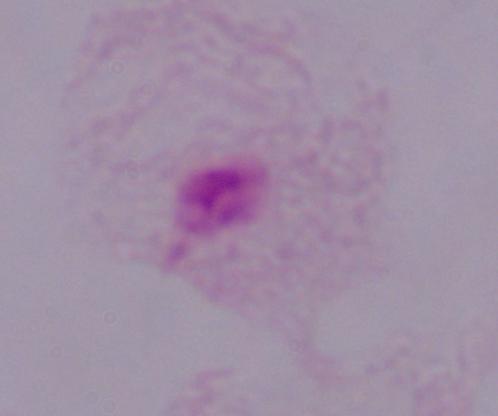
Summary:
  - Identification: trichomonad
  - Modality: micrograph
  - Magnification: 1000x